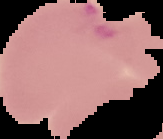

Result: Plasmodium parasites detected. From a thin blood film. The area outside the segmented cell region is set to black. Image is 163×139 pixels.